Give the position of every Plasmodium parasite.
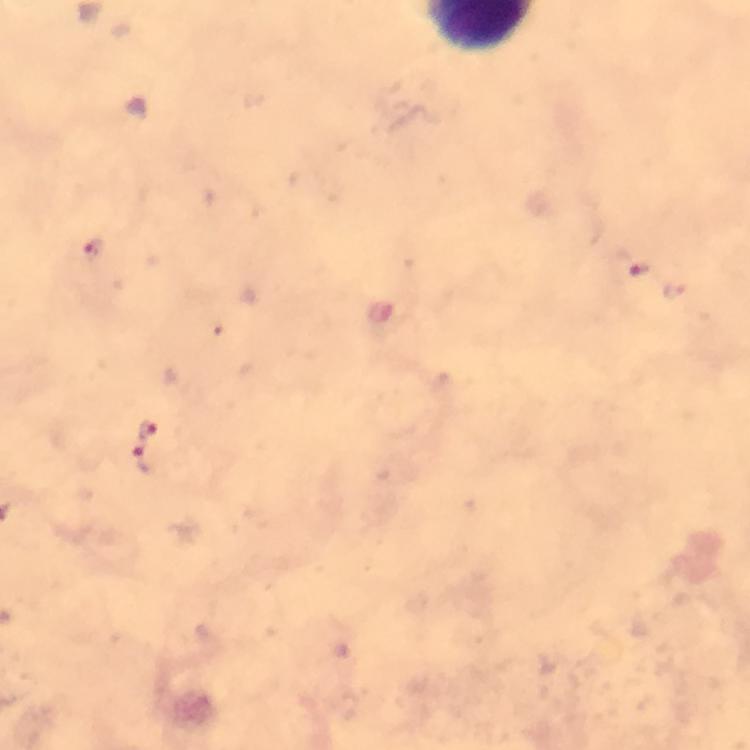
Approximate centers as (x, y) in pixels.
Plasmodium parasites: (93, 249), (634, 267), (145, 430), (144, 460).

Summary:
  - Context: from a diagnostic examination for malaria
  - Capture: smartphone photograph through a microscope
  - Image size: 750×750 pixels
  - Preparation: thick blood smear
  - Cropped from: a single field of view
  - Immersion oil: used
  - Magnification: 100x
  - Stain: Giemsa